Locate every Trypanosoma brucei.
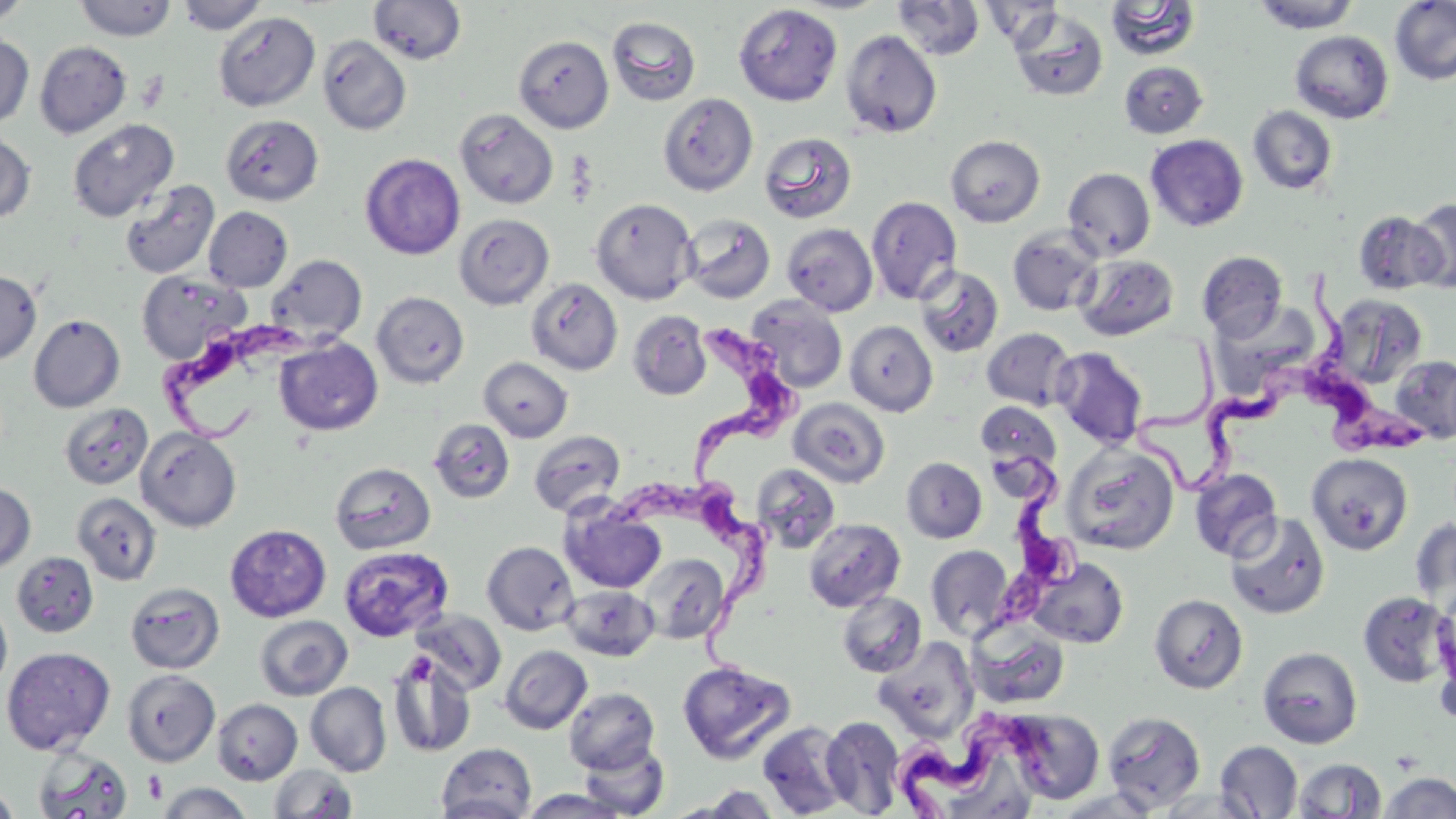
Approximate bounding boxes as (x1,y1)-(x2,y2) corner pairs in pixels.
Trypanosoma brucei: (1295,270)-(1426,460), (690,307)-(803,482), (159,316)-(339,444), (1130,336)-(1325,494), (977,446)-(1087,648), (617,478)-(786,674), (887,696)-(1062,818).

Summary:
  - Uninfected red blood cell locations: (0,0)-(32,27), (74,0)-(177,41), (177,0)-(268,34), (368,0)-(467,64), (1390,0)-(1456,86), (892,1)-(986,60), (979,1)-(1065,49), (1105,1)-(1202,61), (1252,1)-(1362,32), (733,4)-(842,106), (1008,9)-(1108,102), (214,11)-(320,111), (606,16)-(701,106), (841,30)-(942,138), (1290,31)-(1394,124), (0,33)-(34,129), (514,35)-(614,133), (317,36)-(412,135), (34,41)-(132,139), (1119,62)-(1208,139), (658,93)-(758,196), (1247,106)-(1338,195), (455,109)-(558,209), (221,114)-(324,206), (67,118)-(179,222), (0,131)-(36,224), (759,131)-(857,224), (774,132)-(867,316), (1145,134)-(1248,232), (945,135)-(1045,227), (360,153)-(465,259), (1063,167)-(1155,260), (119,179)-(220,279), (866,196)-(962,305), (590,197)-(697,305), (1409,199)-(1456,292), (203,207)-(292,292), (1352,208)-(1445,294), (453,213)-(554,310), (681,214)-(776,303), (782,223)-(878,316), (1007,225)-(1103,316), (1197,251)-(1289,340), (1075,253)-(1180,341), (266,255)-(367,346), (915,265)-(1004,358), (0,271)-(41,365), (137,271)-(250,365), (526,278)-(623,375), (372,291)-(470,388), (1328,294)-(1427,389), (746,295)-(848,393), (627,310)-(712,400), (29,314)-(125,413), (845,321)-(938,417), (981,327)-(1077,411), (275,337)-(383,436), (1051,346)-(1148,449), (1390,355)-(1456,443), (479,357)-(572,442), (788,398)-(890,488), (975,401)-(1061,472), (59,403)-(152,490), (428,419)-(515,503), (136,427)-(242,532), (528,429)-(626,516), (1063,444)-(1179,555), (1306,453)-(1413,555), (901,457)-(987,543), (330,462)-(436,554), (751,463)-(841,554), (1190,468)-(1282,562), (0,483)-(35,571), (72,492)-(162,585), (560,501)-(666,594), (1225,511)-(1330,620), (1411,516)-(1456,618), (803,518)-(906,612), (225,524)-(331,622), (482,541)-(579,635), (926,544)-(1014,641), (339,546)-(453,642), (11,552)-(99,638), (639,553)-(731,643), (1029,557)-(1128,649), (125,581)-(224,674), (561,585)-(659,661), (837,591)-(927,678), (1357,591)-(1455,689), (1149,594)-(1248,694), (1433,594)-(1456,720), (0,597)-(12,694), (412,609)-(506,695), (254,615)-(353,701), (966,618)-(1070,710), (873,638)-(979,741), (500,645)-(592,734), (1,646)-(116,755), (1257,646)-(1363,749), (386,650)-(477,758), (677,660)-(796,764), (122,669)-(220,767), (305,682)-(391,776), (564,687)-(660,774), (212,698)-(302,784), (1005,709)-(1105,804), (1102,711)-(1206,813), (820,716)-(905,816), (757,721)-(851,817), (578,740)-(670,818), (1215,740)-(1303,818), (436,742)-(537,819), (33,745)-(133,819), (1292,759)-(1387,818), (269,764)-(358,819), (1379,772)-(1456,818), (155,782)-(254,818), (0,786)-(20,819), (685,786)-(785,818), (1054,787)-(1163,818), (1154,788)-(1263,818), (518,789)-(633,818)
  - Platelet locations: (405,653)-(436,684), (144,770)-(167,803)
  - Slide-level diagnosis: Trypanosoma brucei
  - Modality: optical microscopy
  - Image size: 1456×819 pixels
  - Field of view: single
  - Preparation: thin blood film
  - Magnification: 1000x
  - Stain: May-Grünwald-Giemsa